Locate every blood parasite and identify its species.
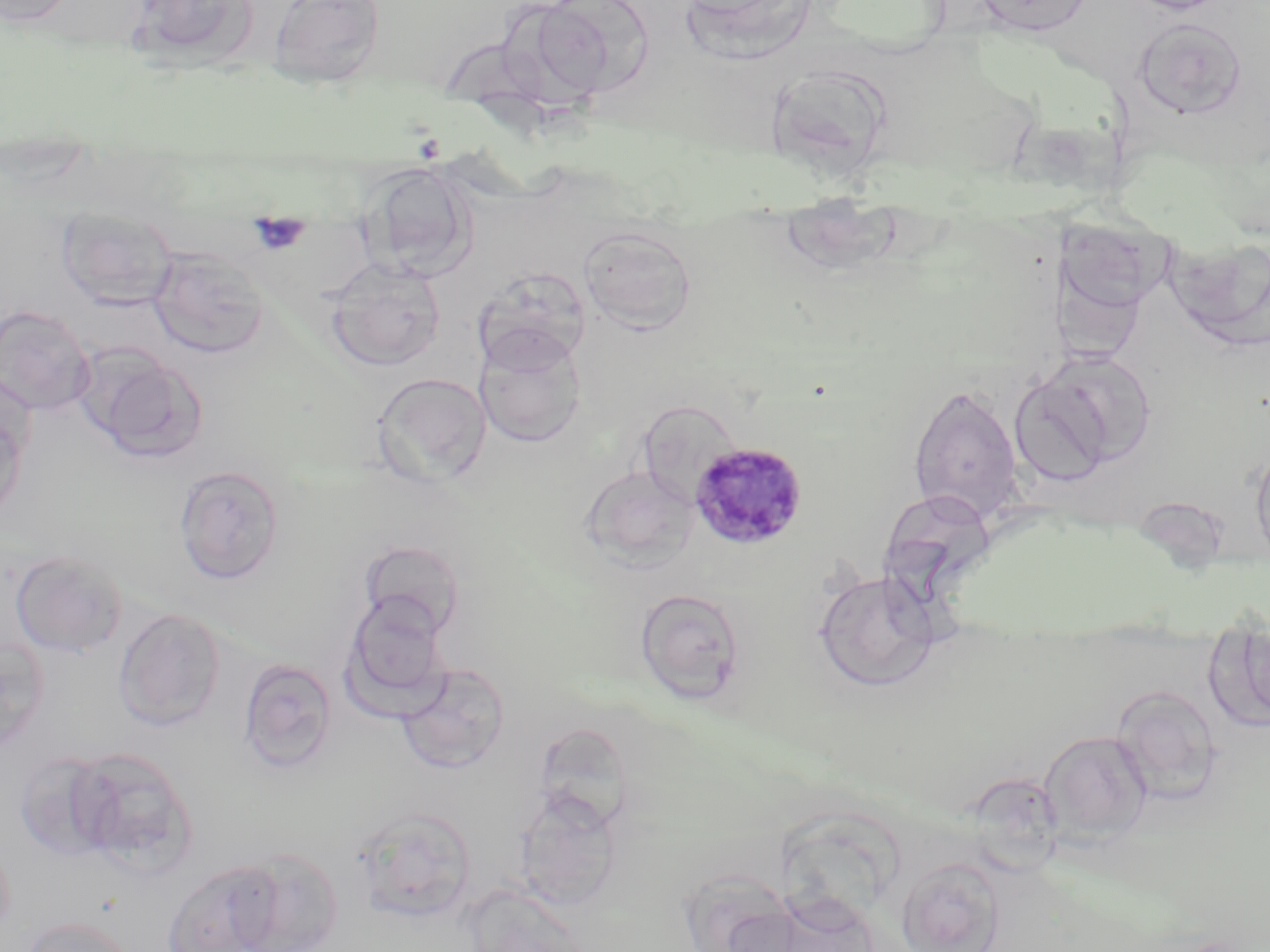
Approximate bounding boxes as (x1,y1)-(x2,y2) corner pairs in pixels.
Plasmodium malariae-infected red blood cells: (688,442)-(808,551).
No Plasmodium falciparum, Plasmodium ovale, Plasmodium vivax, Babesia divergens, or Trypanosoma brucei observed.

Summary:
  - Platelet locations: (249,215)-(310,255)
  - Uninfected red blood cell locations: (0,0)-(78,27), (130,0)-(261,69), (267,0)-(387,88), (676,0)-(819,61), (969,0)-(1094,36), (1123,0)-(1233,15), (524,1)-(652,102), (1133,17)-(1247,118), (766,74)-(904,184), (0,146)-(95,188), (358,161)-(478,279), (55,206)-(179,310), (1052,216)-(1174,323), (577,224)-(698,333), (1164,232)-(1270,350), (148,248)-(269,359), (325,260)-(446,372), (471,267)-(590,373), (0,305)-(95,415), (475,332)-(586,448), (1035,349)-(1157,467), (84,350)-(207,464), (372,372)-(492,486), (1009,373)-(1114,487), (0,379)-(32,526), (908,384)-(1024,524), (636,399)-(743,506), (1250,440)-(1270,566), (173,464)-(285,585), (580,466)-(699,570), (357,538)-(467,641), (10,550)-(128,658), (814,569)-(938,692), (634,588)-(746,702), (341,595)-(452,717), (114,607)-(227,731), (1219,628)-(1270,731), (0,635)-(49,754), (238,657)-(338,774), (397,662)-(510,773), (1111,684)-(1222,802), (1039,731)-(1152,843), (67,745)-(196,874), (15,752)-(117,861), (513,790)-(623,910), (354,807)-(477,921), (230,847)-(345,952), (897,857)-(1005,952), (162,860)-(282,952), (676,867)-(805,952), (463,885)-(592,952), (19,916)-(136,952)
  - Slide-level diagnosis: Plasmodium malariae
  - Preparation: thin blood film
  - Stain: May-Grünwald-Giemsa
  - Field of view: single
  - Modality: light microscopy
  - Image size: 1270×952 pixels
  - Magnification: 1000x